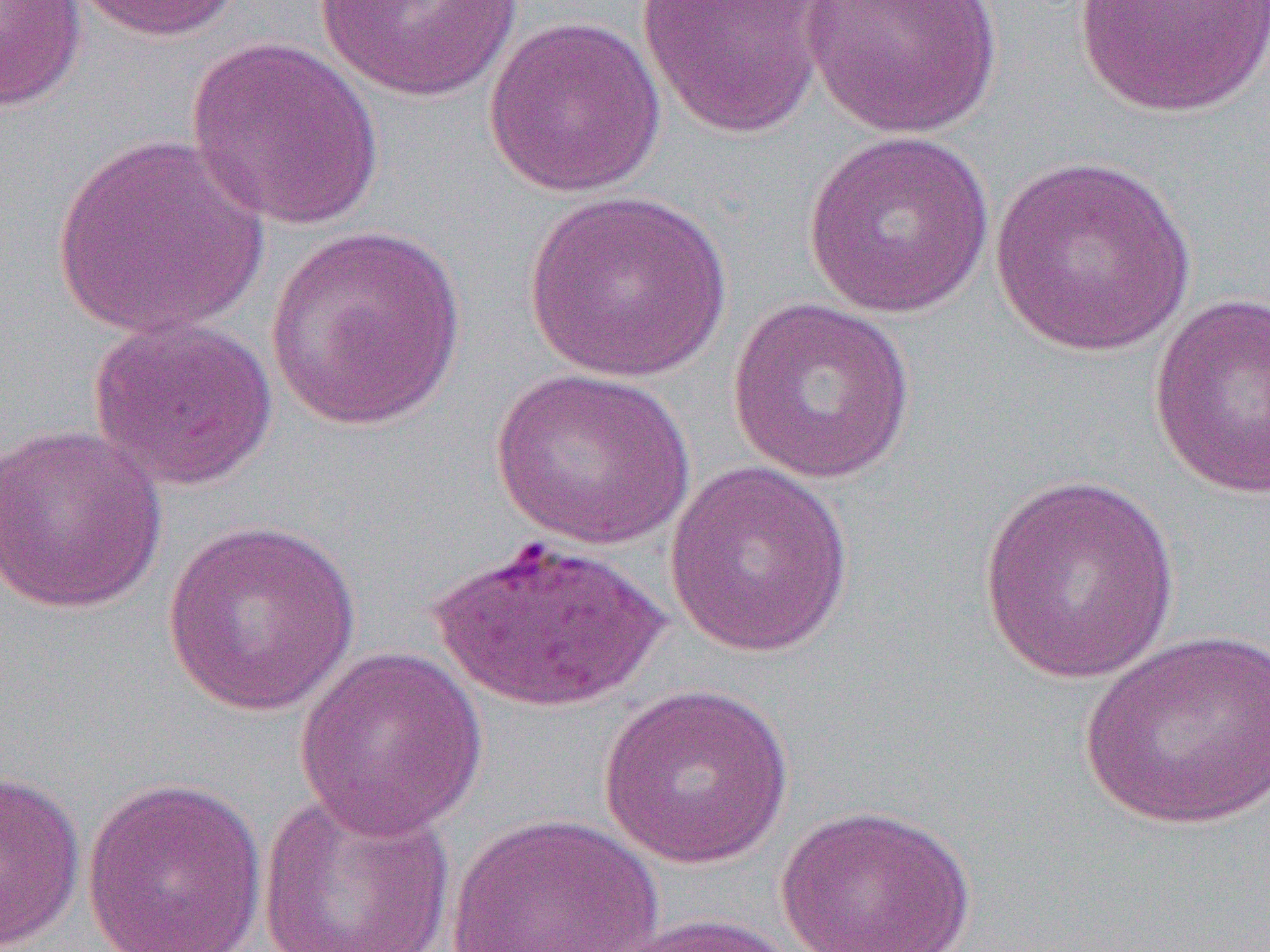
Summary:
  - Coordinate format: approximate bounding boxes as [x1, y1, x2, y2] in pixels
  - Uninfected red blood cell locations: [0, 0, 87, 114], [70, 0, 246, 42], [306, 0, 535, 106], [636, 0, 832, 140], [801, 0, 1005, 139], [1072, 0, 1270, 118], [484, 15, 667, 198], [186, 37, 386, 231], [801, 130, 997, 321], [51, 132, 271, 340], [988, 155, 1198, 358], [522, 188, 734, 385], [264, 226, 467, 431], [1149, 293, 1270, 499], [725, 296, 918, 484], [87, 316, 279, 491], [490, 367, 697, 549], [0, 423, 168, 613], [663, 462, 855, 658], [977, 474, 1183, 686], [162, 519, 362, 717], [430, 533, 671, 714], [1078, 626, 1270, 832], [294, 646, 488, 839], [597, 682, 795, 869], [0, 769, 86, 952], [80, 777, 269, 952], [257, 786, 456, 952], [773, 804, 979, 952], [445, 812, 665, 952], [601, 913, 805, 952]
  - Slide-level diagnosis: Plasmodium falciparum
  - Modality: optical microscopy
  - Image size: 1270×952 pixels
  - Field of view: one of a larger specimen
  - Magnification: 1000x
  - Preparation: thin blood smear